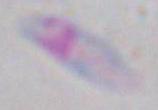 1000x magnification. Toxoplasma gondii is shown. Micrograph.